State which parasite is depicted.
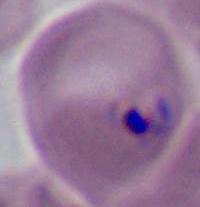
This is Plasmodium.

Summary:
  - Magnification: 400x or 1000x
  - Modality: photomicrograph